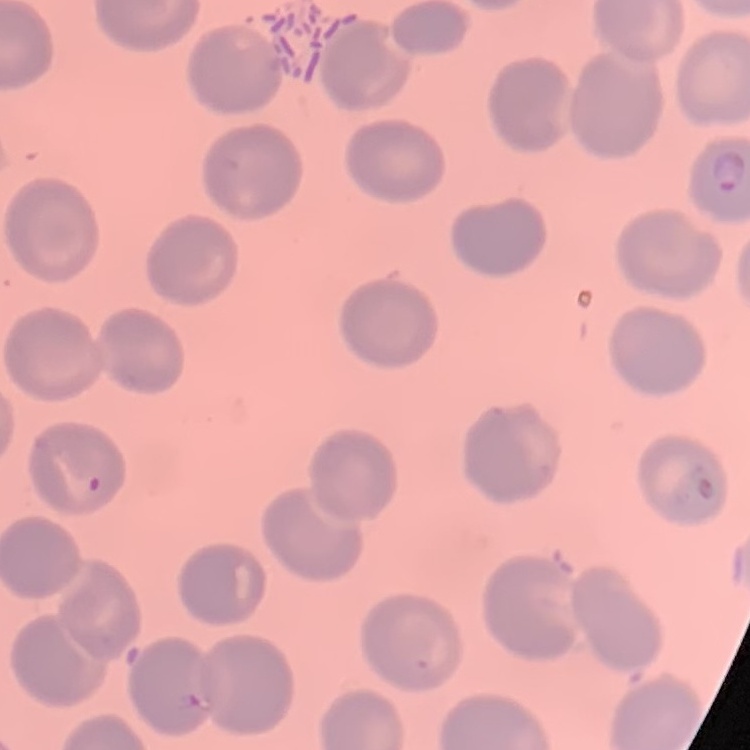

erythrocyte morphology = no rouleaux formation
stain = Field's or Giemsa
image type = one tile cut from a larger photomicrograph
preparation = thin peripheral smear